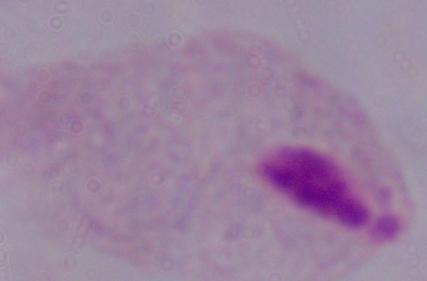

Summary:
  - Identification: trichomonad
  - Modality: micrograph
  - Magnification: 1000x